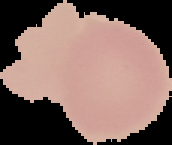
From a thin blood film. Result: negative for Plasmodium parasites. Image is 172×145 pixels. Segmented cell region on a black background.